Locate every blood parasite and identify its species.
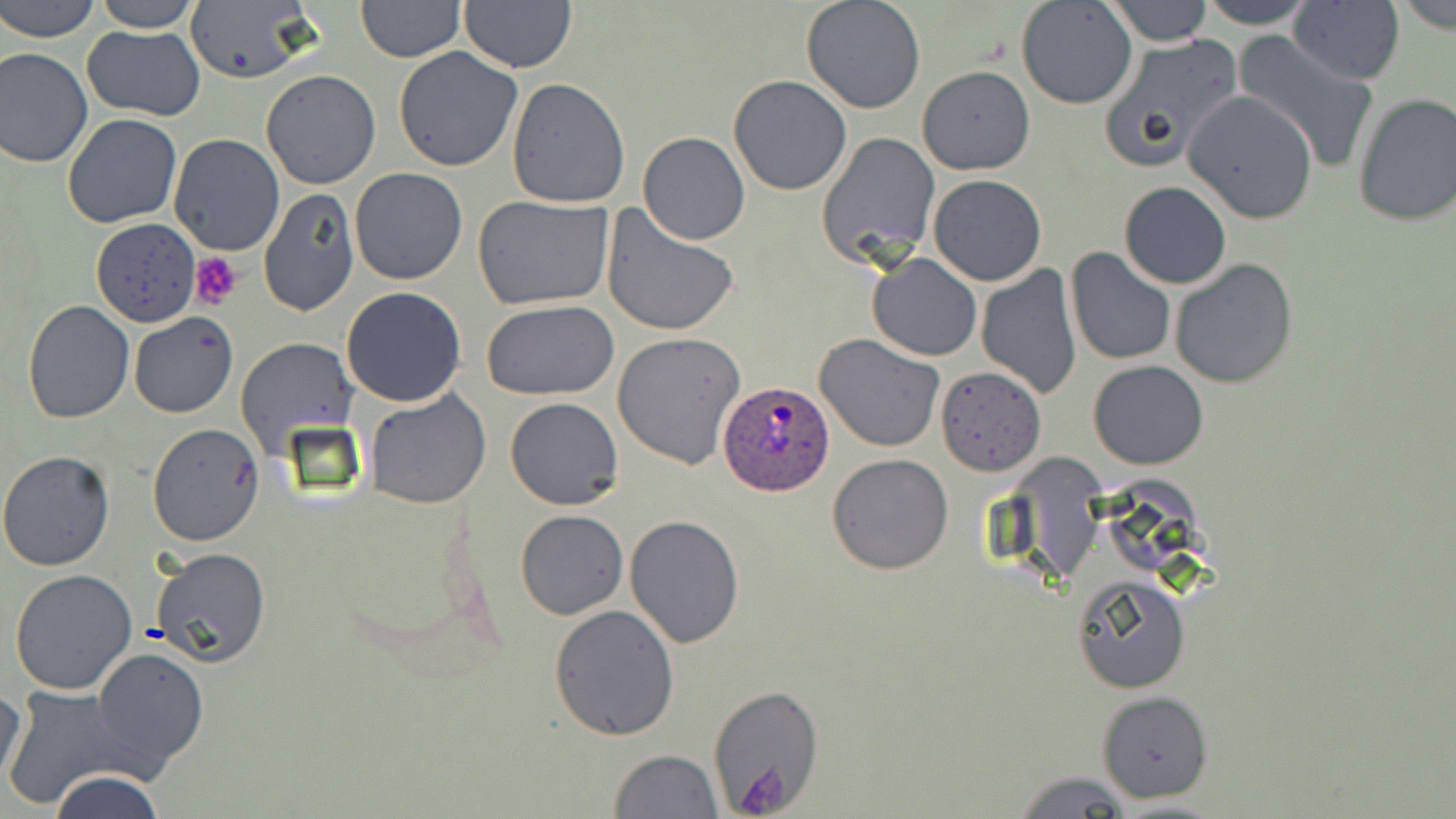

Approximate bounding boxes as (x1, y1, x2, y2) in pixels.
Plasmodium ovale-infected red blood cells: (717, 381, 835, 495).
No Plasmodium falciparum, Plasmodium malariae, Plasmodium vivax, Babesia divergens, or Trypanosoma brucei observed.

Uninfected red blood cell locations: (1, 0, 100, 43), (92, 0, 205, 32), (181, 0, 317, 85), (801, 0, 926, 113), (1016, 0, 1138, 108), (1105, 0, 1213, 46), (1195, 0, 1317, 30), (1289, 0, 1405, 85), (354, 1, 466, 63), (460, 1, 576, 73), (80, 25, 205, 121), (1233, 32, 1380, 173), (1097, 33, 1245, 174), (0, 45, 94, 168), (394, 45, 524, 172), (917, 65, 1035, 175), (260, 69, 382, 190), (728, 75, 852, 195), (506, 78, 633, 208), (1181, 91, 1319, 223), (1352, 92, 1456, 228), (61, 114, 182, 228), (817, 131, 941, 268), (639, 132, 750, 244), (169, 134, 285, 257), (349, 167, 469, 285), (929, 174, 1046, 286), (1118, 180, 1232, 289), (258, 187, 359, 316), (472, 195, 618, 312), (602, 205, 740, 337), (91, 219, 199, 327), (1066, 248, 1175, 365), (866, 252, 981, 361), (1169, 257, 1298, 389), (976, 264, 1081, 399), (340, 287, 468, 407), (480, 298, 620, 400), (22, 301, 134, 424), (129, 312, 238, 419), (614, 331, 745, 469), (814, 334, 945, 454), (235, 337, 357, 454), (1089, 361, 1208, 468), (936, 365, 1047, 477), (364, 388, 492, 509), (505, 396, 625, 510), (147, 423, 264, 546), (0, 450, 117, 571), (826, 454, 952, 575), (515, 510, 627, 618), (625, 515, 744, 649), (151, 545, 271, 666), (8, 567, 139, 696), (1072, 578, 1191, 694), (548, 603, 680, 742), (92, 645, 210, 771), (1, 681, 28, 793), (705, 684, 825, 813), (4, 686, 140, 810), (1098, 689, 1214, 802), (610, 749, 721, 819), (1012, 769, 1133, 818), (48, 770, 167, 819), (1107, 797, 1229, 816). Platelet locations: (189, 251, 246, 310), (736, 758, 800, 816). Slide-level diagnosis: Plasmodium ovale. Thin blood film. Light microscopy. May-Grünwald-Giemsa stain. Single field of view. Image is 1456×819 pixels. Captured at 1000x magnification.